Report the malaria status of this cell.
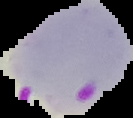
Parasitized.

Summary:
  - Image type: segmented cell region with the area outside set to black
  - Preparation: thin blood film
  - Image size: 133×118 pixels